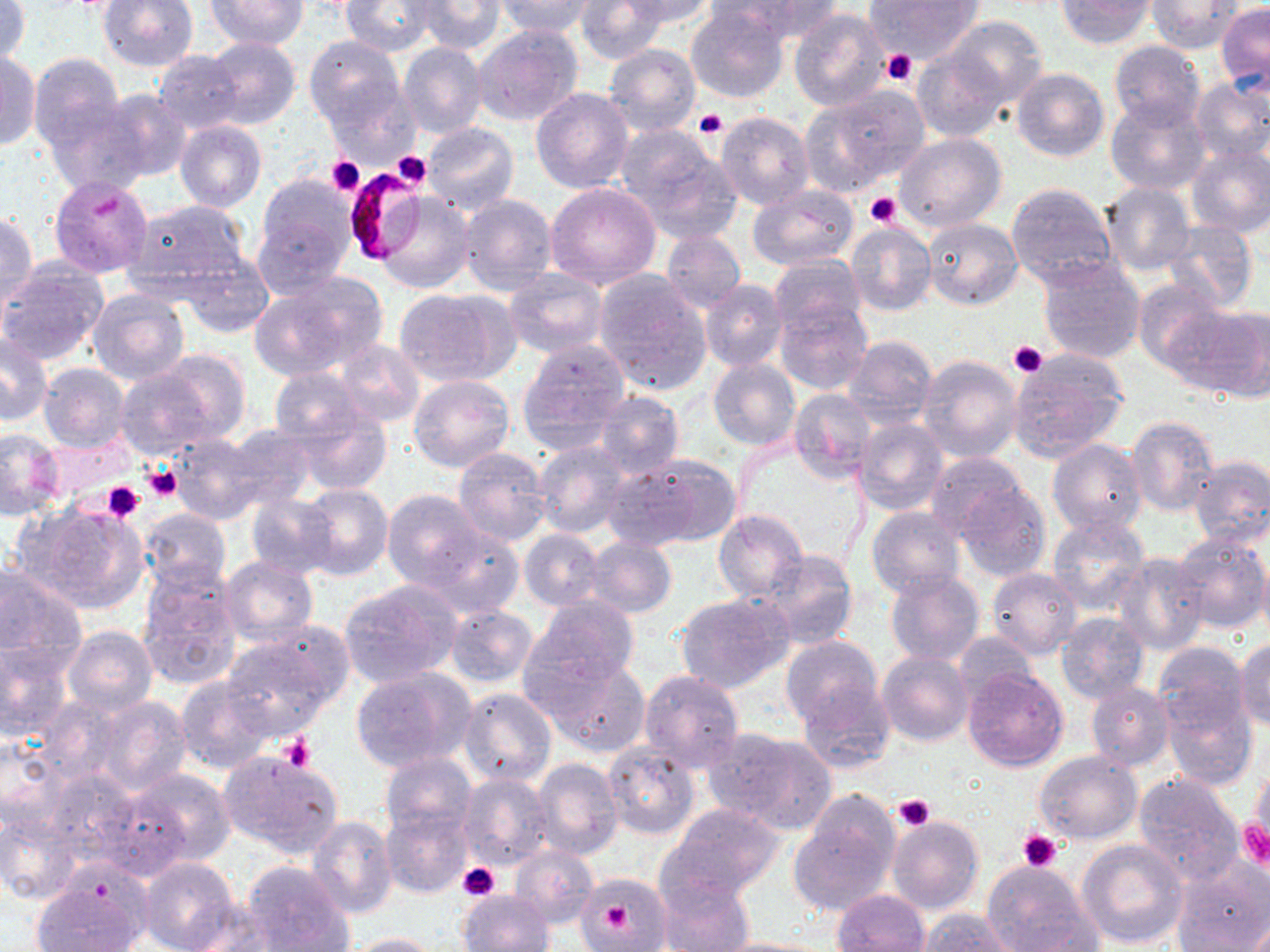

{
  "slide_level_diagnosis": "Plasmodium falciparum",
  "platelet_locations": "approximate bounding boxes as (x1, y1, x2, y2) in pixels: (881, 49, 917, 87), (694, 109, 727, 138), (393, 152, 432, 189), (325, 157, 366, 196), (865, 193, 902, 227), (91, 195, 122, 219), (1007, 341, 1047, 378), (140, 463, 181, 505), (101, 482, 145, 521), (280, 733, 315, 771), (892, 795, 936, 832), (1239, 820, 1270, 869), (1017, 828, 1064, 871), (458, 862, 500, 902), (602, 900, 632, 929)",
  "field_of_view": "single",
  "magnification": "1000x",
  "stain": "May-Grünwald-Giemsa",
  "preparation": "thin blood smear",
  "image_size": "1270×952 pixels",
  "modality": "optical microscopy",
  "uninfected_red_blood_cell_locations": "approximate bounding boxes as (x1, y1, x2, y2) in pixels: (99, 0, 197, 71), (206, 0, 308, 50), (341, 0, 434, 55), (575, 0, 667, 63), (619, 0, 715, 28), (871, 0, 980, 62), (1148, 0, 1242, 52), (0, 1, 31, 64), (414, 1, 506, 54), (495, 1, 594, 39), (723, 1, 839, 42), (1057, 1, 1153, 49), (1217, 3, 1270, 90), (686, 6, 789, 103), (789, 8, 891, 111), (944, 17, 1047, 107), (474, 25, 584, 126), (304, 35, 405, 132), (204, 36, 299, 130), (1108, 40, 1206, 130), (398, 42, 487, 139), (604, 44, 702, 137), (912, 50, 1006, 142), (0, 51, 40, 150), (152, 51, 245, 134), (28, 53, 125, 152), (1011, 67, 1109, 163), (1190, 79, 1270, 166), (531, 87, 632, 191), (809, 88, 930, 190), (100, 89, 192, 181), (1106, 96, 1210, 194), (48, 103, 148, 194), (715, 111, 815, 211), (175, 121, 266, 212), (423, 122, 520, 216), (617, 125, 737, 239), (893, 133, 1006, 233), (1185, 146, 1270, 239), (49, 175, 155, 279), (255, 177, 358, 280), (545, 182, 661, 288), (1006, 182, 1120, 290), (1101, 182, 1195, 277), (747, 186, 858, 269), (374, 192, 475, 292), (459, 193, 558, 298), (121, 199, 249, 303), (1, 211, 38, 313), (923, 218, 1021, 310), (1161, 220, 1260, 313), (476, 221, 576, 338), (845, 223, 936, 316), (660, 229, 746, 314), (178, 252, 276, 337), (769, 255, 866, 339), (1034, 255, 1145, 363), (0, 263, 109, 366), (503, 268, 610, 358), (253, 273, 389, 378), (595, 273, 712, 396), (701, 278, 788, 372), (1133, 280, 1225, 373), (394, 288, 515, 387), (86, 290, 188, 385), (775, 300, 872, 396), (1171, 303, 1270, 401), (0, 332, 53, 426), (843, 334, 937, 426), (517, 339, 632, 447), (333, 340, 425, 427), (149, 349, 251, 444), (1007, 352, 1128, 462), (917, 353, 1025, 462), (708, 357, 800, 450), (38, 361, 131, 454), (114, 365, 227, 460), (269, 366, 375, 449), (408, 374, 516, 473), (789, 389, 875, 482), (594, 390, 684, 478), (289, 403, 394, 496), (1125, 415, 1220, 517), (852, 417, 948, 514), (219, 425, 318, 512), (0, 428, 64, 520), (165, 431, 278, 524), (1047, 439, 1148, 536), (532, 440, 630, 538), (452, 447, 551, 545), (926, 452, 1030, 541), (609, 453, 741, 550), (1188, 455, 1270, 548), (955, 479, 1052, 581), (297, 482, 394, 581), (382, 490, 490, 590), (245, 493, 337, 579), (17, 502, 151, 613), (866, 506, 966, 600), (138, 509, 231, 591), (714, 509, 807, 603), (1047, 515, 1152, 615), (416, 526, 527, 618), (518, 528, 604, 611), (1173, 530, 1268, 634), (583, 537, 677, 617), (1257, 546, 1270, 644), (757, 549, 860, 651), (1112, 552, 1210, 655), (220, 556, 318, 646), (0, 562, 86, 672), (136, 563, 244, 689), (987, 567, 1081, 660), (886, 571, 984, 665), (338, 580, 462, 688), (676, 592, 794, 693), (527, 596, 638, 692), (443, 604, 537, 688), (1056, 612, 1150, 705), (62, 625, 157, 716), (220, 627, 348, 737), (954, 630, 1038, 704), (780, 635, 884, 735), (1192, 637, 1270, 739), (1235, 637, 1270, 732), (0, 642, 74, 743), (878, 651, 974, 747), (541, 656, 650, 757), (961, 664, 1069, 772), (1157, 665, 1258, 786), (350, 668, 473, 776), (639, 669, 744, 771), (175, 675, 276, 775), (798, 679, 897, 774), (1087, 682, 1175, 772), (458, 688, 556, 789), (88, 695, 194, 797), (706, 728, 837, 833), (0, 736, 67, 832), (602, 743, 700, 838), (218, 750, 343, 856), (1034, 752, 1142, 845), (380, 753, 477, 843), (532, 757, 623, 861), (42, 764, 139, 863), (122, 768, 238, 869), (456, 772, 556, 871), (1133, 772, 1245, 884), (1248, 773, 1269, 848), (91, 788, 194, 881), (789, 799, 900, 913), (661, 802, 787, 900), (383, 807, 474, 898), (0, 811, 84, 904), (306, 814, 398, 920), (885, 814, 984, 914), (1076, 838, 1188, 950), (510, 846, 599, 927), (137, 857, 239, 952), (241, 861, 354, 952), (1172, 862, 1270, 951), (982, 864, 1097, 952), (30, 869, 148, 952), (656, 869, 756, 951), (578, 871, 668, 952), (458, 890, 553, 952), (832, 890, 931, 952), (179, 897, 287, 951), (914, 909, 1017, 952), (334, 932, 442, 952), (706, 936, 832, 952)",
  "plasmodium_falciparum_infected_red_blood_cell_locations": "approximate bounding boxes as (x1, y1, x2, y2) in pixels: (341, 169, 426, 266)"
}